State which cell type is depicted.
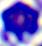

This is a leukocyte.

{
  "modality": "micrograph",
  "magnification": "400x"
}